Classify this cell by malaria status.
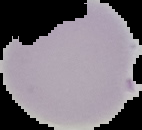

It is uninfected.

Summary:
  - Image size: 142×130 pixels
  - Image type: segmented cell region with the area outside set to black
  - Preparation: thin blood smear